Assess for malaria.
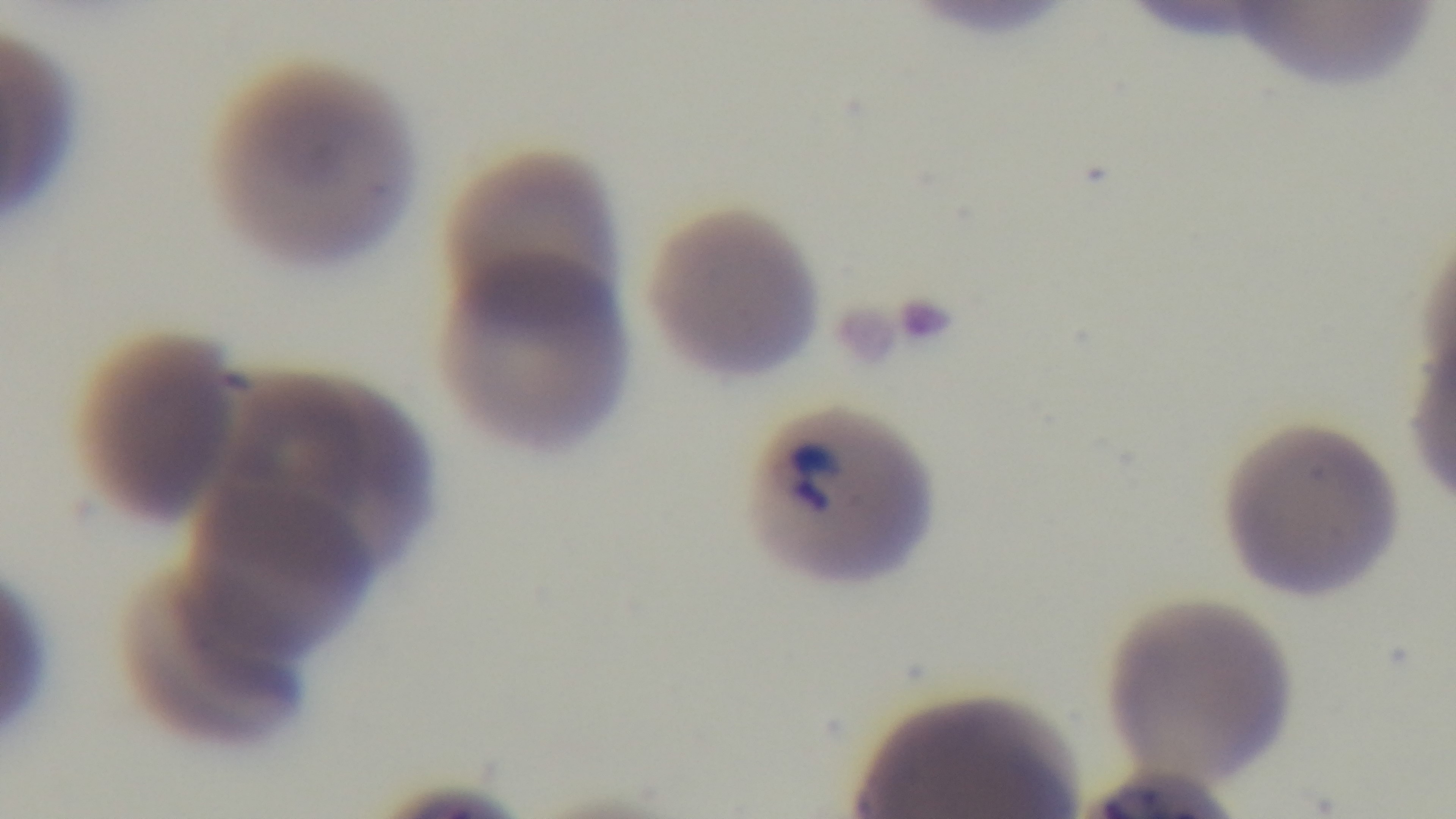

Infected.

Summary:
  - Modality: light microscopy
  - Objective: 100x oil immersion
  - Preparation: thin smear
  - Capture: mounted 4K digital camera
  - Field of view: one from the slide
  - Stain: Giemsa